Report the malaria status of this cell.
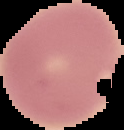
It is uninfected.

From a thin blood film. The area outside the segmented cell region is set to black. Image is 124×130 pixels.